Assess this cell for malaria.
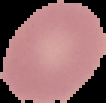
Uninfected.

Segmented cell region on a black background. From a thin blood film. Image is 106×103 pixels.